Describe the morphology of the red blood cells.
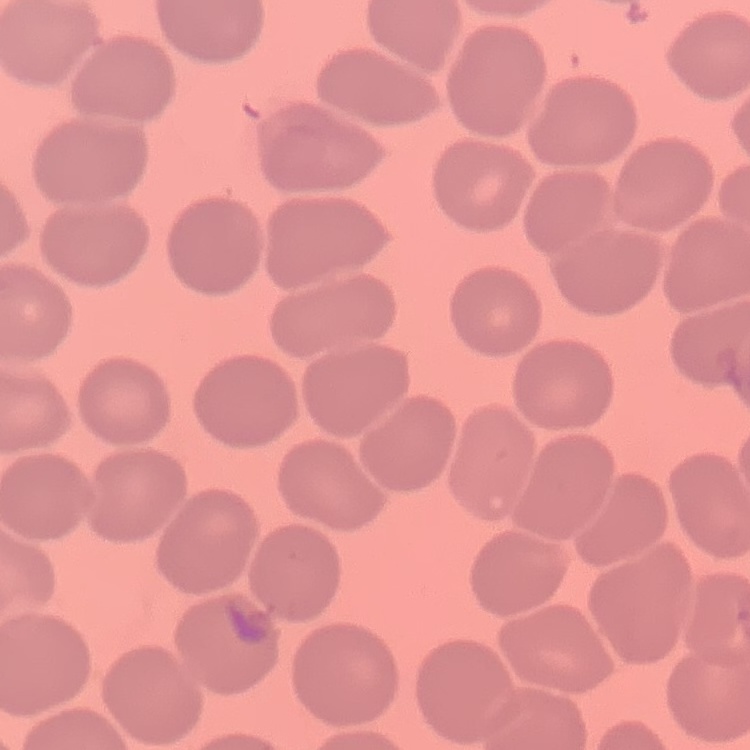

They show no rouleaux formation.

Summary:
  - Stain: Field's or Giemsa
  - Image type: one tile cut from a larger photomicrograph
  - Preparation: thin blood smear